Name the cell type shown.
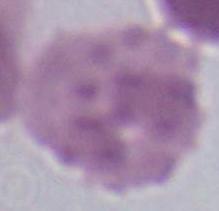

This is an erythrocyte.

magnification: 1000x
modality: photomicrograph